Locate every blood parasite and identify its species.
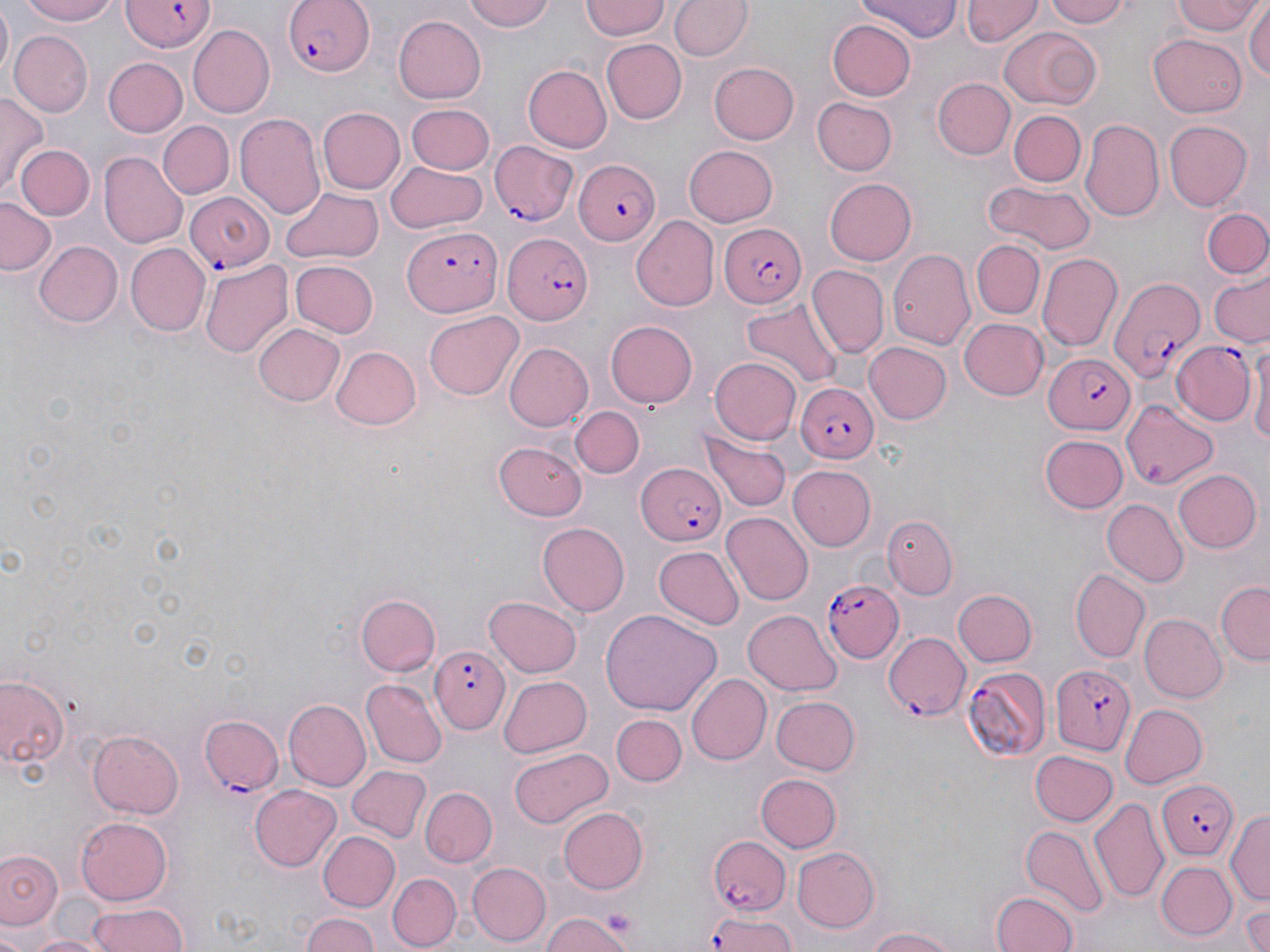

Approximate bounding boxes as (x1, y1, x2, y2) in pixels.
Plasmodium falciparum-infected red blood cells: (117, 0, 218, 51), (284, 0, 373, 77), (492, 140, 579, 225), (570, 151, 661, 251), (185, 191, 274, 273), (721, 223, 806, 306), (402, 228, 502, 315), (502, 232, 592, 324), (1105, 275, 1201, 383), (1171, 341, 1255, 426), (1042, 351, 1133, 434), (797, 383, 877, 464), (634, 463, 728, 547), (824, 579, 904, 661), (885, 632, 968, 717), (428, 646, 509, 735), (1052, 664, 1135, 754), (962, 665, 1053, 760), (199, 715, 286, 796), (1156, 779, 1240, 860), (705, 832, 791, 918), (705, 912, 799, 952).
No Plasmodium ovale, Plasmodium malariae, Plasmodium vivax, Babesia divergens, or Trypanosoma brucei observed.

Summary:
  - Uninfected red blood cell locations: (15, 0, 128, 26), (459, 0, 555, 33), (581, 0, 670, 41), (670, 0, 752, 61), (859, 0, 961, 40), (962, 0, 1044, 48), (1042, 0, 1137, 27), (1170, 0, 1264, 38), (1247, 3, 1270, 87), (1, 6, 13, 79), (392, 15, 487, 103), (827, 19, 917, 100), (186, 24, 275, 118), (997, 25, 1101, 113), (11, 30, 92, 117), (1148, 33, 1248, 118), (600, 38, 685, 123), (105, 58, 188, 137), (709, 61, 798, 144), (522, 65, 612, 153), (934, 76, 1015, 161), (1, 91, 46, 198), (810, 97, 897, 176), (405, 104, 496, 174), (316, 106, 404, 196), (1010, 109, 1086, 187), (235, 113, 324, 220), (1081, 117, 1164, 223), (158, 120, 235, 199), (1164, 120, 1252, 210), (14, 143, 93, 221), (682, 144, 778, 227), (100, 151, 188, 248), (387, 161, 487, 231), (825, 178, 917, 265), (982, 180, 1096, 255), (281, 183, 384, 265), (0, 197, 56, 276), (1204, 210, 1269, 280), (631, 216, 719, 312), (971, 238, 1045, 320), (33, 240, 122, 327), (124, 242, 209, 337), (888, 248, 973, 349), (1039, 251, 1123, 353), (199, 257, 292, 359), (291, 261, 378, 338), (807, 265, 888, 359), (1209, 276, 1269, 347), (741, 298, 844, 390), (424, 310, 525, 400), (959, 318, 1050, 401), (606, 320, 699, 408), (252, 323, 343, 407), (1248, 331, 1270, 452), (503, 342, 593, 431), (865, 342, 953, 424), (329, 345, 421, 429), (709, 355, 801, 442), (1123, 399, 1216, 490), (571, 404, 646, 479), (701, 427, 789, 512), (1040, 434, 1128, 514), (495, 440, 589, 520), (789, 464, 875, 551), (1174, 470, 1261, 554), (1103, 499, 1185, 586), (723, 512, 812, 607), (883, 513, 957, 600), (537, 522, 630, 614), (653, 546, 745, 628), (1072, 570, 1149, 662), (1215, 579, 1270, 666), (954, 587, 1036, 666), (357, 593, 441, 677), (484, 596, 581, 678), (600, 609, 719, 718), (743, 610, 842, 695), (1139, 614, 1226, 702), (687, 672, 772, 766), (0, 673, 70, 772), (499, 673, 593, 756), (361, 678, 447, 769), (772, 696, 860, 775), (282, 700, 370, 790), (1121, 703, 1207, 789), (611, 715, 685, 786), (87, 729, 183, 820), (509, 746, 611, 828), (1029, 749, 1116, 825), (346, 766, 431, 844), (756, 773, 841, 852), (249, 783, 342, 872), (422, 787, 495, 867), (1089, 796, 1169, 904), (558, 807, 650, 894), (1226, 808, 1270, 905), (74, 816, 174, 907), (1021, 826, 1109, 917), (317, 830, 399, 912), (791, 846, 882, 934), (0, 848, 62, 933), (469, 860, 550, 945), (1156, 860, 1237, 940), (387, 873, 459, 950), (990, 890, 1083, 951), (1241, 902, 1270, 952), (83, 903, 190, 951), (542, 910, 638, 952), (300, 911, 383, 952), (859, 926, 964, 952), (20, 933, 107, 952)
  - Slide-level diagnosis: Plasmodium falciparum
  - Modality: optical microscopy
  - Image size: 1270×952 pixels
  - Stain: May-Grünwald-Giemsa
  - Magnification: 1000x
  - Field of view: one of a larger specimen
  - Preparation: thin blood film